Identify the preparation type.
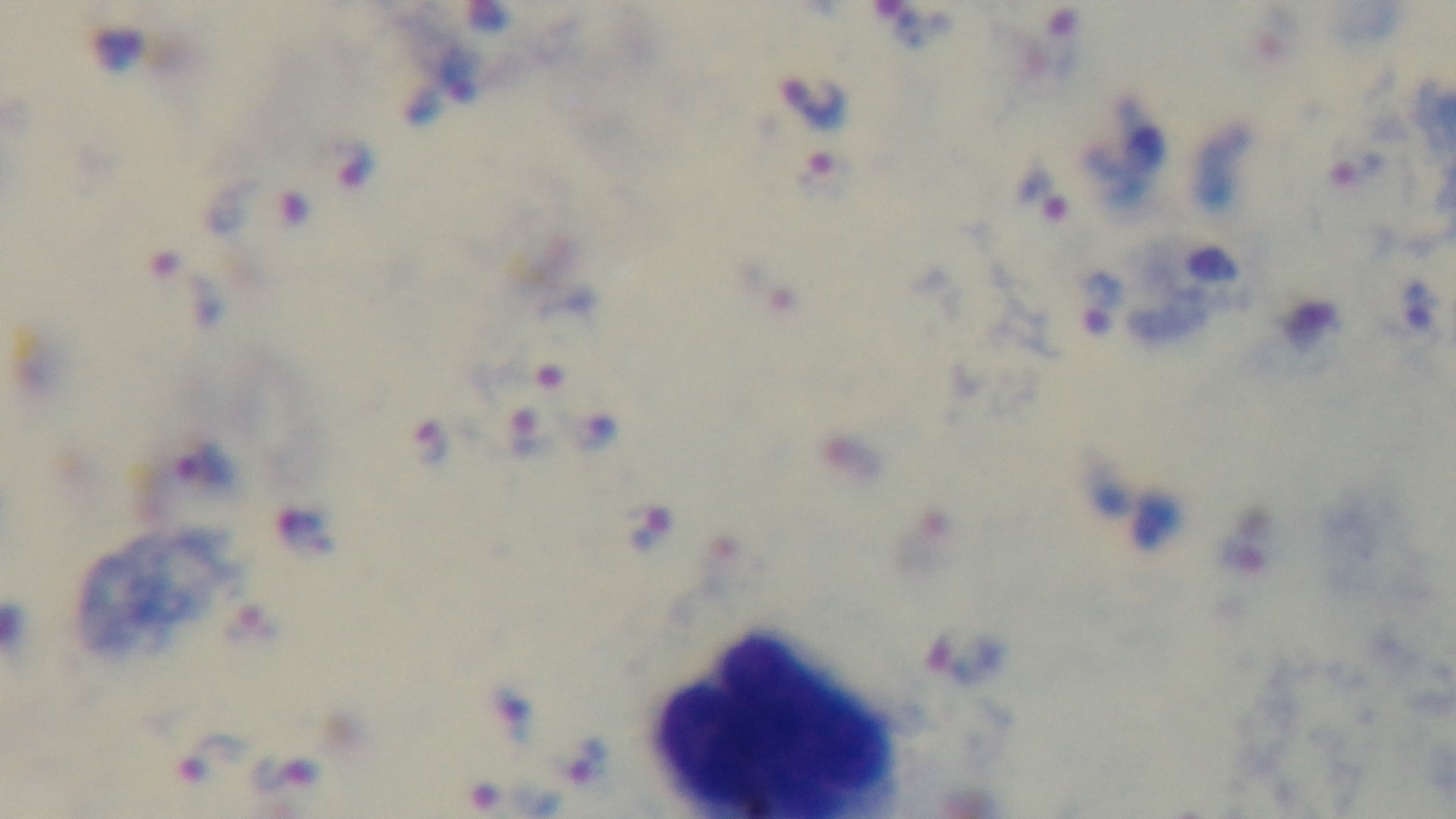
Thick.

field of view = single
stain = Giemsa
modality = light microscopy
objective = 100x oil immersion
malaria status = infected
capture = mounted 4K digital camera